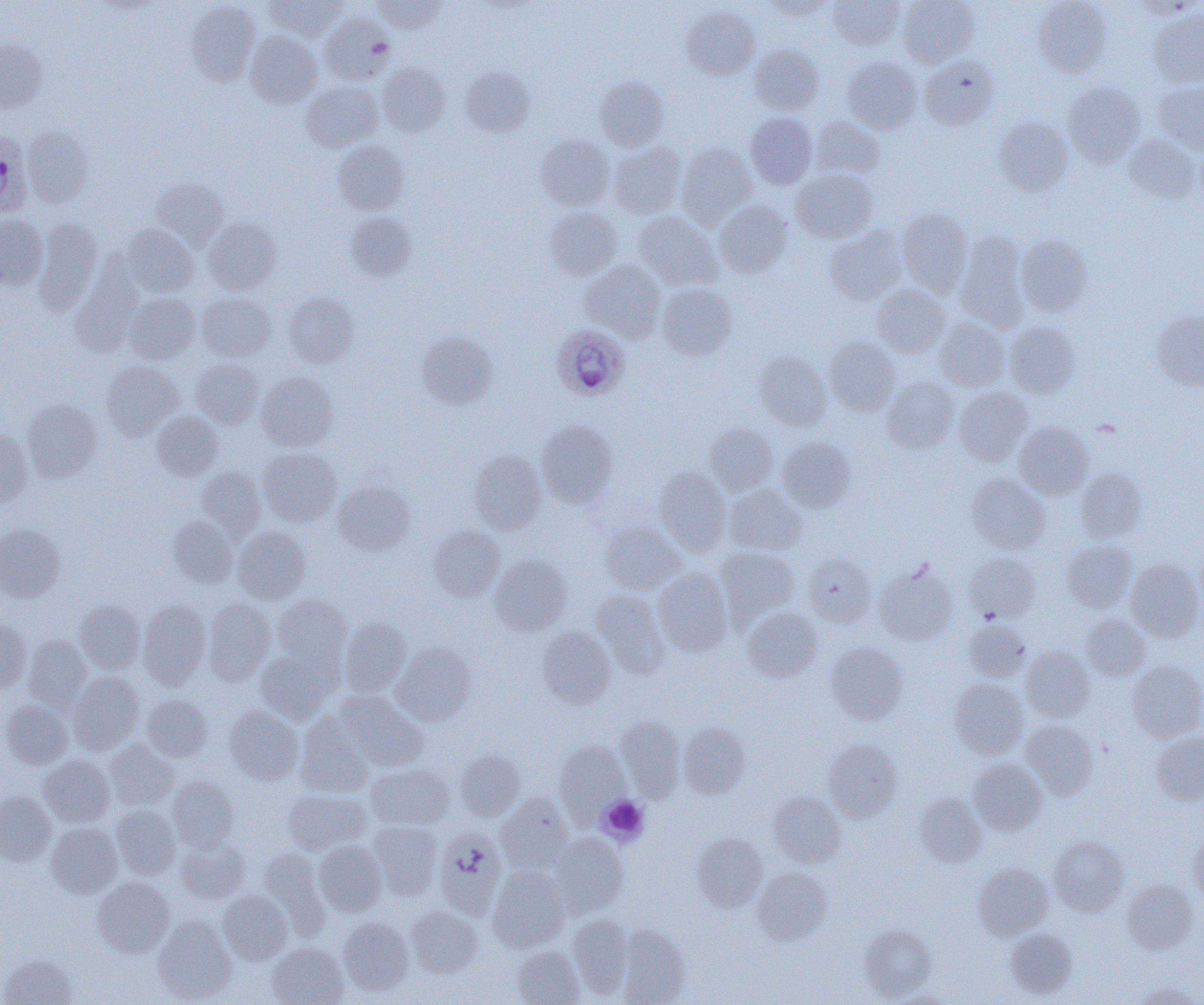 Approximate bounding boxes as (x1,y1)-(x2,y2) corner pairs in pixels. Plasmodium ovale-infected red blood cell locations: (0,130)-(32,219), (551,324)-(629,400). Uninfected red blood cell locations: (265,0)-(347,41), (371,0)-(447,33), (762,0)-(834,20), (828,0)-(904,50), (898,0)-(980,67), (1033,0)-(1111,77), (186,1)-(261,86), (1135,1)-(1200,19), (681,6)-(759,80), (1149,10)-(1204,87), (319,12)-(394,84), (245,31)-(322,108), (0,40)-(48,114), (749,44)-(824,115), (921,54)-(1000,130), (842,57)-(922,134), (377,63)-(450,137), (460,66)-(535,137), (595,76)-(669,151), (301,80)-(383,152), (1155,81)-(1204,152), (1063,82)-(1146,167), (746,113)-(817,189), (810,117)-(884,179), (993,117)-(1073,196), (22,126)-(93,208), (535,134)-(614,210), (1124,134)-(1200,204), (333,140)-(409,214), (609,143)-(685,218), (676,143)-(756,228), (792,168)-(877,243), (151,177)-(228,248), (714,200)-(792,278), (545,207)-(622,280), (896,208)-(973,297), (634,211)-(722,290), (346,212)-(416,281), (0,214)-(48,290), (32,218)-(102,315), (203,218)-(281,294), (122,224)-(198,297), (825,226)-(906,305), (955,230)-(1030,332), (1016,235)-(1093,316), (580,259)-(666,342), (72,265)-(143,357), (657,284)-(737,360), (872,284)-(951,358), (284,291)-(358,367), (124,292)-(200,364), (197,292)-(276,362), (1151,310)-(1204,391), (935,317)-(1010,392), (1005,321)-(1080,397), (416,331)-(497,410), (824,338)-(900,416), (754,352)-(832,430), (191,359)-(264,428), (101,360)-(184,440), (256,371)-(339,451), (882,376)-(959,453), (953,386)-(1033,466), (23,400)-(102,482), (152,412)-(222,480), (536,420)-(618,507), (705,422)-(779,495), (1014,422)-(1093,500), (0,426)-(33,507), (778,437)-(856,512), (258,446)-(341,527), (469,450)-(546,534), (654,466)-(731,554), (196,467)-(266,541), (1075,468)-(1146,543), (966,473)-(1050,554), (333,480)-(415,555), (724,485)-(807,556), (169,516)-(238,588), (601,521)-(686,595), (0,525)-(65,602), (428,525)-(505,602), (233,527)-(310,604), (1062,540)-(1136,612), (715,546)-(800,624), (803,553)-(876,627), (965,553)-(1041,621), (490,555)-(571,635), (1125,557)-(1203,642), (874,563)-(957,645), (653,568)-(734,656), (591,590)-(670,678), (273,594)-(352,669), (203,598)-(275,684), (75,600)-(144,674), (138,600)-(211,690), (743,608)-(823,681), (1081,614)-(1150,681), (339,618)-(412,697), (0,619)-(31,692), (963,619)-(1030,682), (536,627)-(616,708), (23,635)-(91,711), (392,642)-(476,726), (825,642)-(908,724), (1021,646)-(1094,721), (255,651)-(332,723), (1127,661)-(1204,742), (67,671)-(144,754), (950,678)-(1028,759), (335,690)-(428,770), (142,694)-(213,761), (1,699)-(73,769), (224,706)-(303,784), (295,714)-(373,796), (616,716)-(686,801), (1022,720)-(1099,799), (679,722)-(751,799), (1150,731)-(1204,805), (823,739)-(903,822), (104,740)-(179,810), (554,740)-(630,821), (455,750)-(525,821), (39,755)-(114,827), (968,759)-(1047,835), (366,763)-(454,829), (167,775)-(238,851), (283,788)-(371,854), (0,790)-(55,866), (768,791)-(846,867), (496,793)-(573,874), (914,793)-(986,867), (111,804)-(181,879), (368,820)-(442,899), (46,822)-(122,898), (435,828)-(507,919), (551,833)-(628,917), (691,833)-(768,912), (1188,833)-(1204,904), (1049,835)-(1129,915), (175,837)-(249,902), (315,840)-(386,917), (259,848)-(329,936), (973,863)-(1053,940), (488,866)-(570,952), (753,867)-(832,946), (92,877)-(174,958), (1122,879)-(1198,953), (218,890)-(292,964), (407,905)-(483,978), (567,914)-(634,998), (153,916)-(236,1004), (337,917)-(413,995), (616,924)-(690,1005), (860,924)-(936,1000), (1005,927)-(1077,999), (267,942)-(348,1005), (512,946)-(584,1004), (1,954)-(77,1004), (1131,982)-(1202,1005). Platelet locations: (597,794)-(649,846). Slide-level diagnosis: Plasmodium ovale. Thin blood film. Optical microscopy. Image is 1204×1005 pixels. Single field of view. Captured at 1000x magnification.